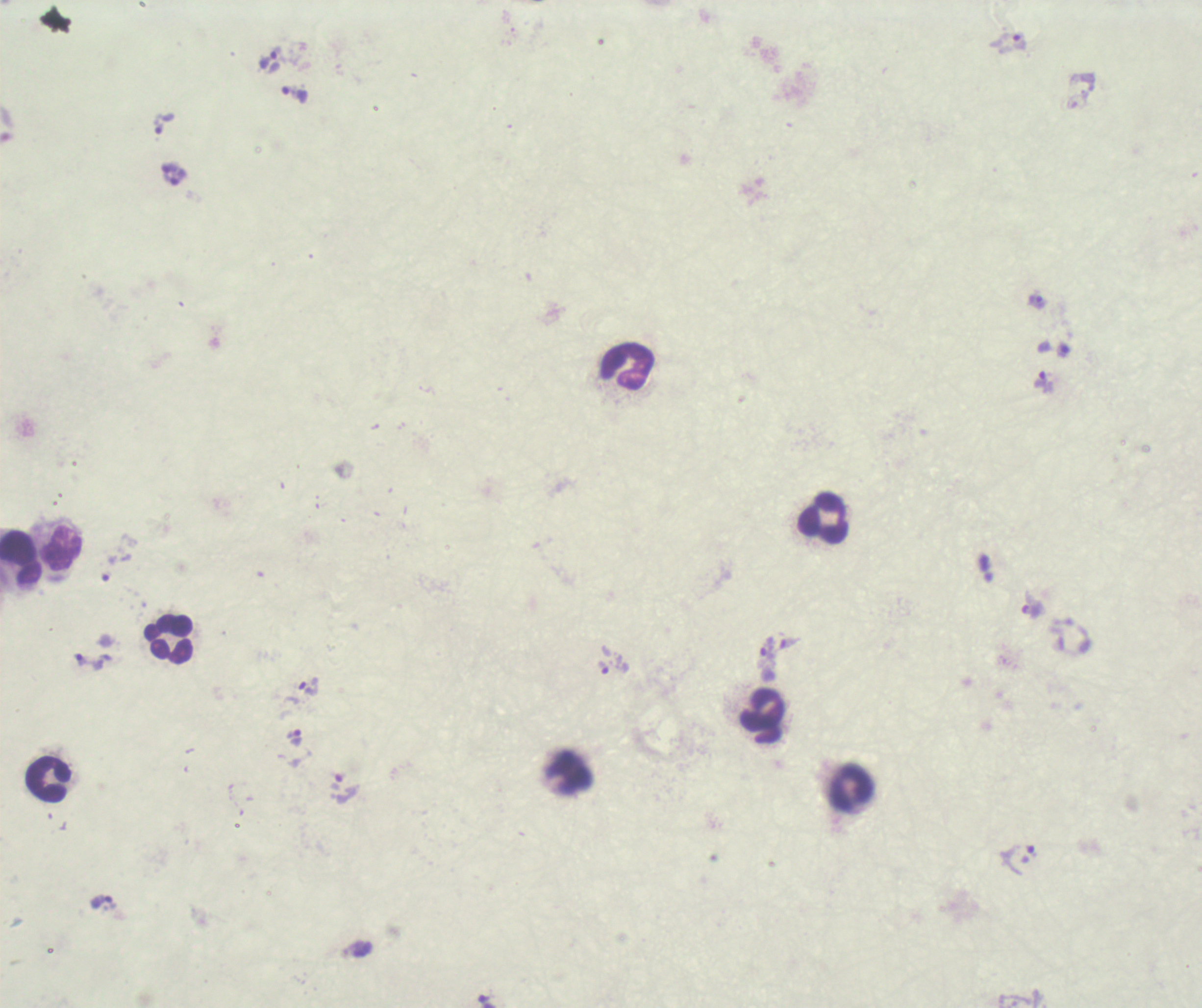
Approximate centers as (x, y) in pixels. Trophozoite locations: (1007, 42), (268, 60), (293, 95), (165, 122), (1037, 303), (1043, 382), (766, 651), (88, 661), (603, 668), (309, 687), (295, 738), (1031, 850). Leukocyte locations: (626, 367), (823, 519), (63, 549), (21, 558), (170, 640), (762, 718), (47, 780), (850, 788). Image is 1202×1008 pixels. Thick blood film. Result: positive for Plasmodium parasites. Background quality: poor. Previously used in an actual diagnosis. Romanowsky-stained preparation. One field from this slide. Coloration quality: bad. 100x magnification.